Report the malaria status of this cell.
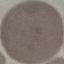
It is uninfected.

Cell patch, automatically extracted from a larger field of view and resized to 64 × 64 pixels. Giemsa stain. Acquired by smartphone through the microscope eyepiece. Thin blood smear.